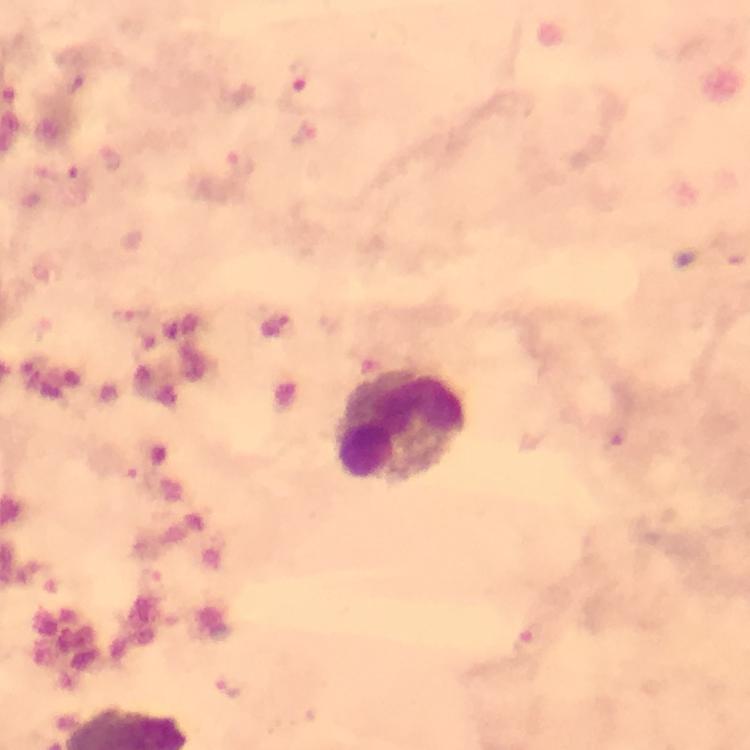

context: from a diagnostic examination for malaria
capture: smartphone camera through the microscope
leukocyte_locations: 'approximate centers as {x, y} in pixels: {402, 426}'
preparation: thick smear
stain: Giemsa
immersion_oil: applied
magnification: 100x
cropped_from: one field of view
image_size: 750×750 pixels
malaria_parasite_locations: 'approximate centers as {x, y} in pixels: {300, 76}, {242, 162}, {78, 181}, {129, 318}, {613, 445}, {135, 477}, {152, 584}, {528, 642}, {232, 686}'